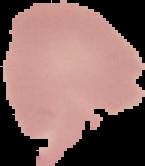
Summary:
  - Image size: 145×166 pixels
  - Preparation: thin blood film
  - Result: no malaria parasites detected
  - Image type: segmented cell region with the area outside set to black